Assess this cell for malaria.
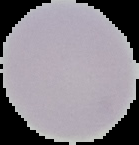
It is uninfected.

Cell region segmented out of the field of view; the surrounding area is masked to black. Image is 139×145 pixels. From a thin blood film.